Classify this cell by malaria status.
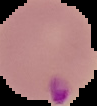

Parasitized.

{
  "preparation": "thin blood film",
  "image_size": "97×106 pixels",
  "image_type": "segmented cell region with the area outside set to black"
}